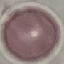
{
  "result": "negative for malaria parasites",
  "preparation": "thin blood film",
  "stain": "Giemsa",
  "capture": "smartphone through the microscope eyepiece",
  "image_type": "automatically extracted cell patch, resized to 64 × 64 pixels"
}